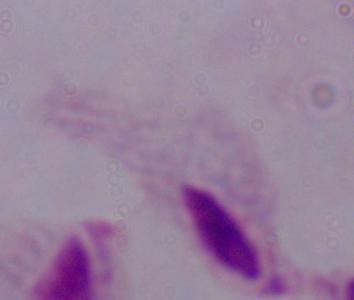

Summary:
  - Magnification: 1000x
  - Identification: trichomonad
  - Modality: photomicrograph